Locate every blood parasite and identify its species.
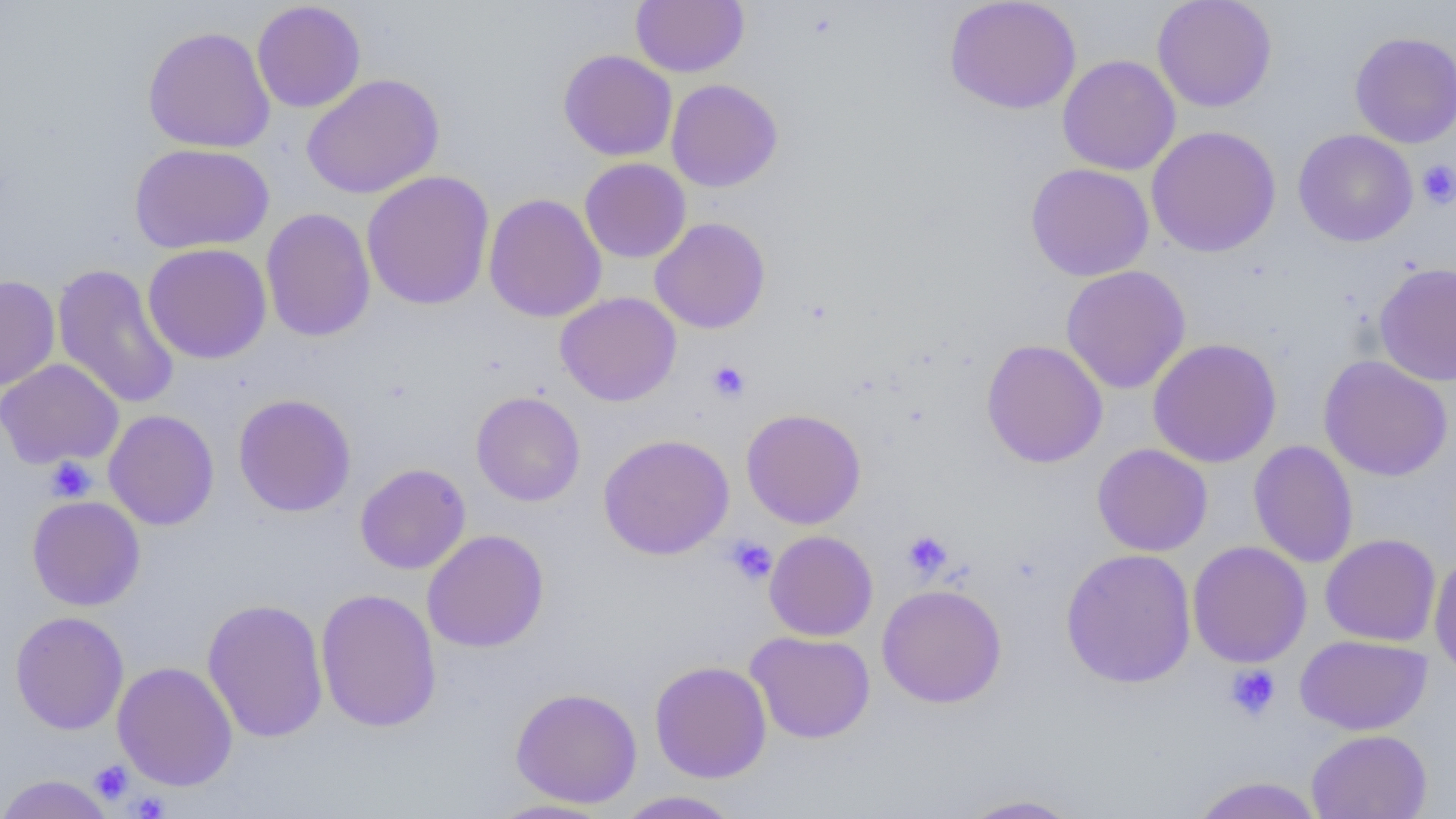
No blood parasites observed.

Approximate bounding boxes as [x1, y1, x2, y2] in pixels. Uninfected red blood cell locations: [631, 0, 749, 77], [944, 0, 1082, 114], [1151, 0, 1277, 112], [251, 1, 366, 113], [142, 25, 276, 153], [1349, 30, 1456, 148], [558, 49, 677, 162], [1058, 54, 1181, 175], [302, 73, 444, 199], [666, 79, 783, 192], [1146, 125, 1281, 258], [1293, 129, 1418, 247], [130, 142, 275, 254], [579, 158, 691, 263], [1025, 163, 1154, 281], [362, 170, 495, 310], [483, 193, 607, 323], [260, 207, 376, 342], [650, 217, 771, 334], [142, 243, 272, 364], [1374, 261, 1456, 387], [52, 263, 180, 410], [1061, 265, 1191, 394], [0, 275, 60, 392], [555, 291, 681, 407], [1147, 337, 1282, 468], [981, 339, 1108, 468], [1317, 355, 1454, 481], [0, 358, 124, 469], [471, 391, 585, 507], [232, 394, 357, 517], [741, 408, 866, 529], [103, 409, 220, 531], [598, 433, 734, 559], [1248, 441, 1359, 568], [1092, 443, 1213, 556], [355, 463, 471, 574], [27, 496, 146, 611], [422, 529, 549, 653], [764, 530, 878, 641], [1320, 533, 1441, 646], [1187, 540, 1312, 668], [1060, 548, 1196, 689], [1429, 554, 1456, 681], [877, 583, 1007, 708], [315, 588, 442, 733], [202, 598, 329, 743], [10, 611, 129, 735], [745, 631, 876, 744], [1295, 634, 1432, 736], [649, 660, 772, 783], [112, 661, 238, 791], [510, 687, 643, 808], [1306, 729, 1432, 819], [0, 774, 116, 819], [1188, 776, 1326, 819], [613, 790, 744, 818], [957, 793, 1086, 818], [487, 798, 617, 818]. Platelet locations: [1417, 159, 1456, 209], [706, 360, 751, 403], [46, 456, 96, 502], [902, 530, 952, 579], [724, 536, 777, 586], [1225, 664, 1281, 722], [90, 760, 133, 803], [128, 791, 169, 818]. Slide-level diagnosis: negative for blood parasites. Captured at 1000x magnification. Thin blood film. Light microscopy. Image is 1456×819 pixels. One field of a larger specimen.